Mark where cells are.
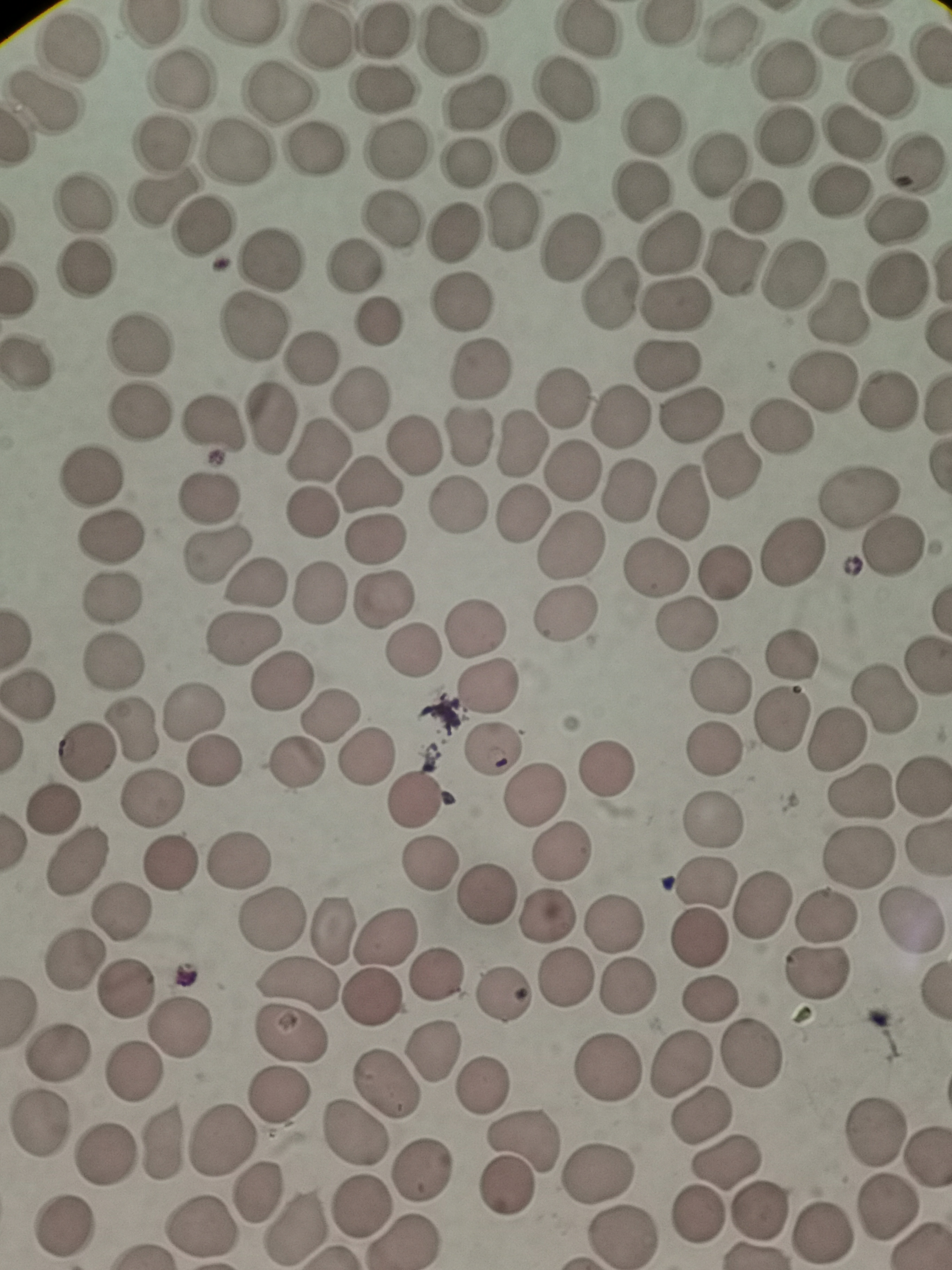
Approximate centers as [x, y] in pixels.
Cells: [851, 32], [385, 33], [586, 33], [324, 36], [729, 38], [453, 39], [72, 48], [782, 73], [182, 80], [886, 85], [384, 91], [567, 92], [280, 96], [41, 99], [475, 102], [653, 124], [853, 135], [784, 137], [163, 142], [528, 142], [397, 151], [315, 152], [236, 154], [466, 162], [917, 163], [717, 164], [638, 190], [841, 194], [161, 197], [86, 203], [761, 205], [392, 217], [900, 217], [512, 218], [203, 226], [452, 230], [668, 243], [569, 246], [269, 259], [735, 265], [354, 266], [84, 270], [795, 275], [901, 279], [611, 294], [462, 300], [677, 303], [839, 315], [377, 321], [139, 344], [311, 357], [25, 363], [667, 366], [479, 370], [823, 382], [562, 395], [360, 398], [888, 399], [139, 411], [691, 416], [622, 418], [269, 421], [212, 426], [782, 430], [469, 435], [521, 443], [414, 444], [311, 453], [732, 466], [574, 468], [92, 473], [366, 484], [630, 490], [859, 497], [209, 499], [681, 502], [458, 506], [308, 513], [521, 513], [111, 537], [376, 540], [571, 547], [895, 547], [213, 554], [793, 554], [655, 570], [725, 573], [256, 581], [315, 594], [386, 595], [112, 598], [567, 613], [476, 623], [687, 624], [247, 639], [411, 649], [794, 651], [114, 661], [279, 684], [487, 684], [720, 685], [27, 694], [883, 697], [331, 711], [192, 712], [782, 717], [134, 728], [835, 740], [715, 747], [494, 749], [85, 752], [362, 756], [216, 760], [295, 764], [607, 769], [922, 785], [858, 787], [534, 795], [153, 800], [418, 801], [52, 808], [712, 819], [560, 853], [859, 858], [77, 860], [240, 861], [429, 862], [169, 863], [703, 885], [484, 893], [765, 905], [119, 912], [544, 912], [273, 918], [828, 918], [913, 921], [614, 924], [333, 931], [389, 937], [697, 941], [73, 960], [823, 975], [437, 976], [565, 977], [293, 982], [626, 984], [126, 993], [504, 995], [709, 1001], [184, 1030], [292, 1034], [434, 1050], [752, 1052], [58, 1053], [684, 1060], [611, 1066], [128, 1073], [482, 1082], [389, 1083], [278, 1097], [700, 1114], [41, 1126], [873, 1132], [353, 1133], [218, 1137], [159, 1144], [521, 1144], [104, 1157], [730, 1160], [424, 1168], [597, 1170], [506, 1185], [255, 1191], [362, 1203], [759, 1208], [888, 1209], [701, 1217], [204, 1228], [294, 1229], [63, 1230], [821, 1232], [622, 1237], [403, 1242].

Summary:
  - Stain: Giemsa
  - Image size: 952×1270 pixels
  - Field of view: single
  - Capture: smartphone through the microscope eyepiece
  - Preparation: thin blood smear